Locate every Trypanosoma brucei.
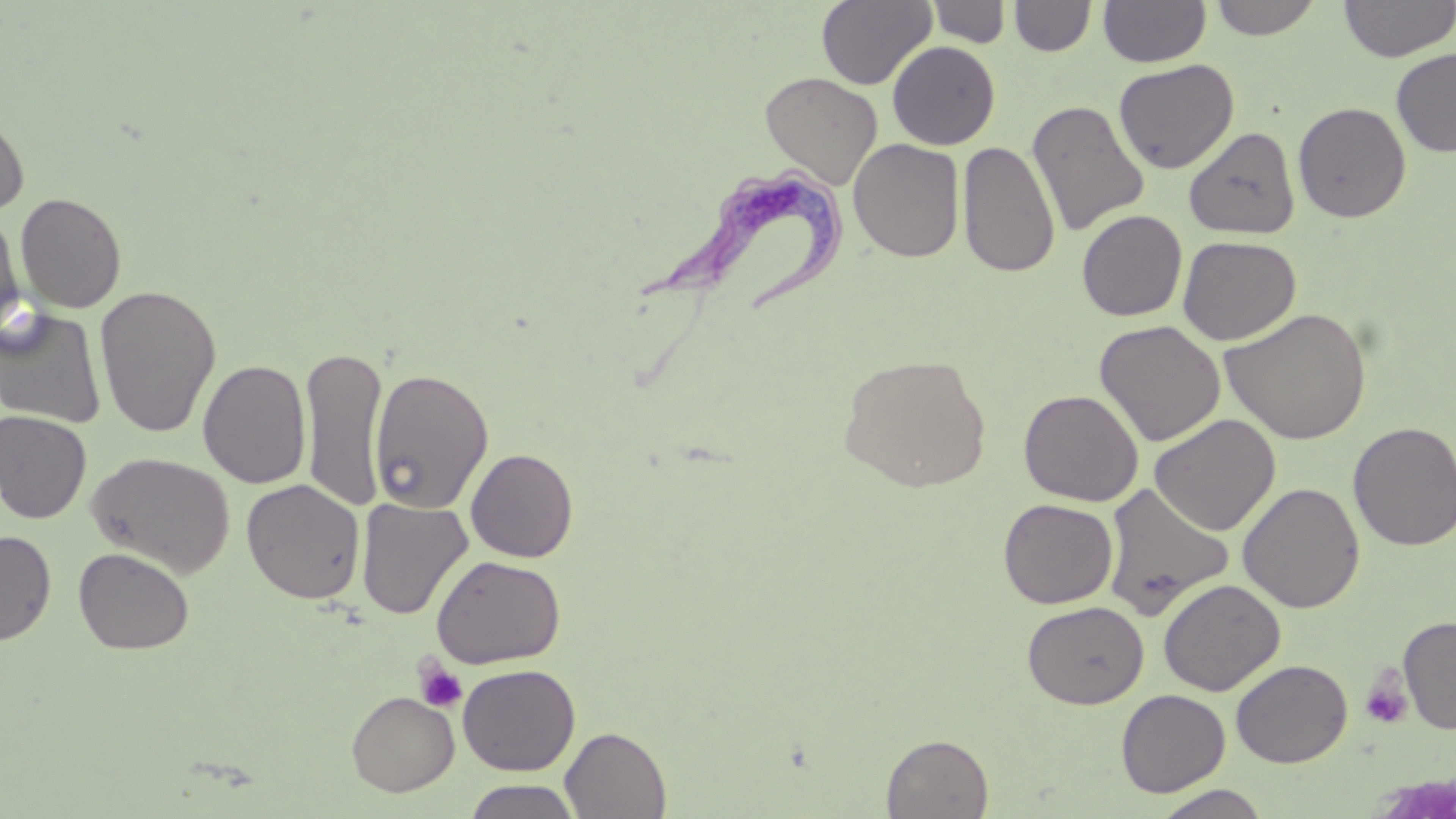
Approximate bounding boxes as [x1, y1, x2, y2] in pixels.
Trypanosoma brucei: [642, 166, 853, 314].

Platelet locations: [415, 659, 467, 713], [1359, 669, 1413, 729]. Uninfected red blood cell locations: [816, 0, 937, 89], [1009, 0, 1097, 57], [1098, 0, 1211, 67], [1208, 0, 1324, 40], [1338, 0, 1456, 62], [927, 1, 1012, 48], [887, 41, 1000, 149], [1391, 48, 1456, 157], [1113, 59, 1239, 174], [760, 71, 883, 189], [1026, 99, 1149, 237], [1293, 101, 1412, 223], [0, 113, 30, 217], [1183, 126, 1301, 239], [848, 139, 965, 263], [958, 140, 1059, 278], [15, 192, 127, 313], [1, 209, 26, 339], [1077, 209, 1188, 322], [1178, 235, 1301, 345], [95, 285, 221, 437], [1219, 306, 1371, 445], [0, 307, 107, 429], [1094, 319, 1226, 447], [299, 345, 387, 510], [837, 353, 991, 492], [198, 359, 311, 488], [369, 368, 494, 513], [1019, 389, 1143, 506], [0, 410, 92, 523], [1149, 413, 1281, 536], [1348, 421, 1456, 551], [466, 448, 579, 562], [87, 451, 236, 578], [241, 478, 366, 604], [1101, 482, 1234, 619], [1238, 482, 1364, 613], [356, 497, 473, 620], [998, 498, 1118, 608], [0, 530, 56, 645], [73, 547, 194, 655], [431, 555, 567, 669], [1158, 578, 1285, 696], [1022, 600, 1149, 709], [1397, 615, 1456, 734], [1231, 659, 1352, 768], [457, 663, 580, 775], [1116, 689, 1231, 796], [346, 690, 459, 796], [560, 727, 671, 818], [881, 733, 994, 818], [462, 779, 584, 819], [1151, 785, 1274, 819]. Slide-level diagnosis: Trypanosoma brucei. Light microscopy. 1000x magnification. Thin blood smear. Image is 1456×819 pixels. One field of a larger specimen. May-Grünwald-Giemsa-stained preparation.